Locate and identify every blood parasite.
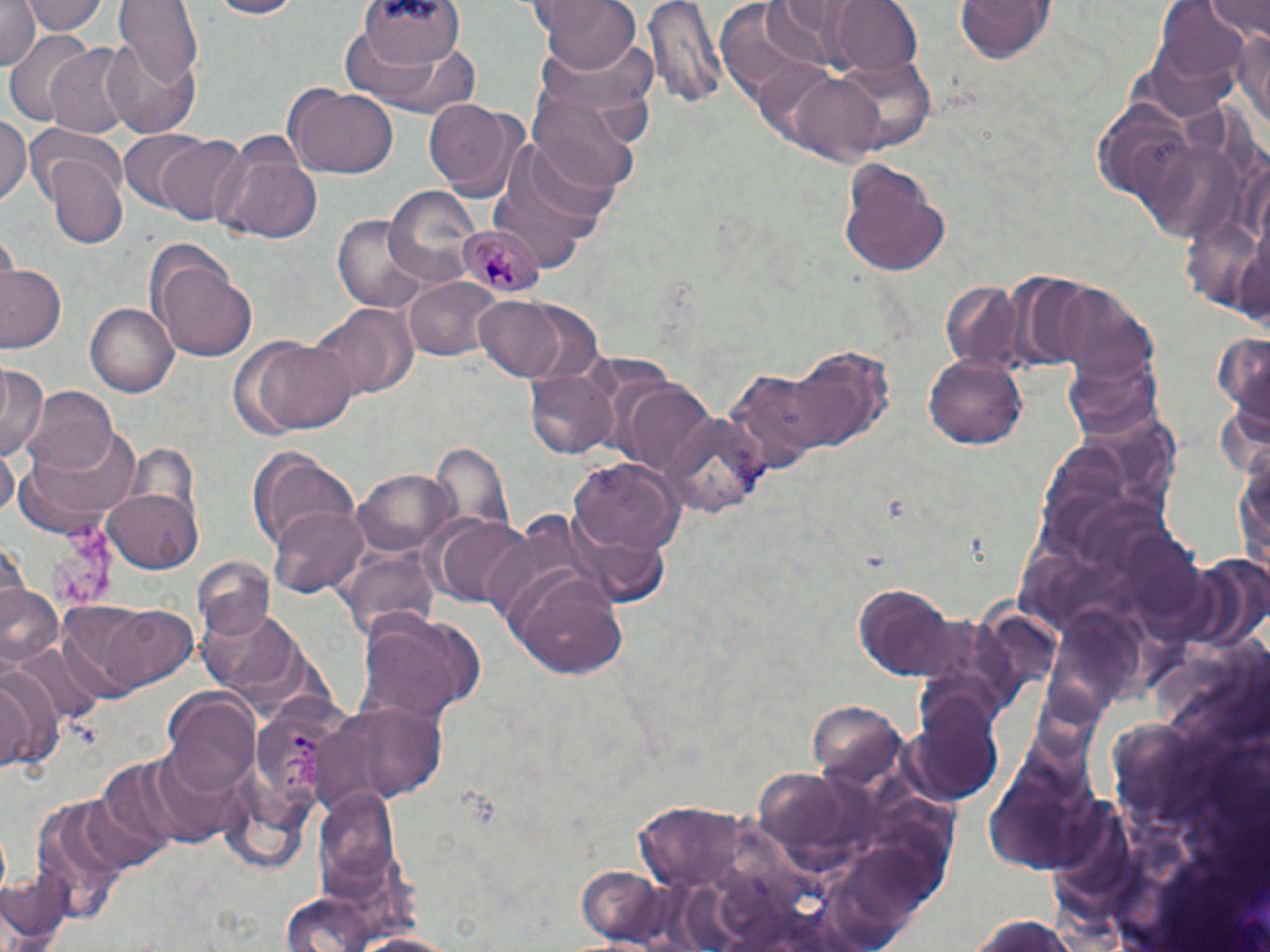
Approximate bounding boxes as named x1/y1/x2/y2 corners in pixels.
Plasmodium malariae-infected red blood cells: (x1=456, y1=224, x2=547, y2=302).
No Plasmodium falciparum, Plasmodium ovale, Plasmodium vivax, Babesia divergens, or Trypanosoma brucei observed.

Uninfected red blood cell locations: (x1=23, y1=0, x2=106, y2=37), (x1=114, y1=0, x2=202, y2=87), (x1=202, y1=0, x2=303, y2=19), (x1=358, y1=0, x2=463, y2=71), (x1=537, y1=0, x2=640, y2=73), (x1=647, y1=0, x2=725, y2=111), (x1=953, y1=0, x2=1057, y2=66), (x1=1157, y1=0, x2=1254, y2=83), (x1=1203, y1=0, x2=1270, y2=39), (x1=833, y1=1, x2=925, y2=75), (x1=0, y1=2, x2=40, y2=74), (x1=1232, y1=20, x2=1270, y2=134), (x1=4, y1=31, x2=101, y2=125), (x1=102, y1=33, x2=203, y2=142), (x1=349, y1=35, x2=480, y2=121), (x1=44, y1=44, x2=135, y2=141), (x1=834, y1=51, x2=939, y2=155), (x1=783, y1=71, x2=893, y2=166), (x1=286, y1=84, x2=399, y2=179), (x1=528, y1=93, x2=637, y2=198), (x1=423, y1=98, x2=517, y2=192), (x1=0, y1=116, x2=29, y2=209), (x1=25, y1=126, x2=123, y2=208), (x1=119, y1=131, x2=208, y2=208), (x1=156, y1=136, x2=247, y2=226), (x1=214, y1=144, x2=323, y2=244), (x1=47, y1=154, x2=129, y2=249), (x1=837, y1=159, x2=951, y2=277), (x1=386, y1=185, x2=482, y2=285), (x1=332, y1=217, x2=438, y2=313), (x1=156, y1=252, x2=258, y2=362), (x1=1, y1=264, x2=65, y2=353), (x1=403, y1=276, x2=501, y2=363), (x1=938, y1=280, x2=1024, y2=374), (x1=1048, y1=282, x2=1157, y2=384), (x1=471, y1=294, x2=573, y2=383), (x1=86, y1=303, x2=178, y2=397), (x1=313, y1=304, x2=419, y2=401), (x1=240, y1=332, x2=357, y2=437), (x1=1211, y1=334, x2=1270, y2=416), (x1=923, y1=353, x2=1027, y2=449), (x1=0, y1=365, x2=46, y2=460), (x1=525, y1=369, x2=619, y2=460), (x1=24, y1=390, x2=118, y2=478), (x1=14, y1=423, x2=146, y2=538), (x1=248, y1=445, x2=360, y2=561), (x1=0, y1=446, x2=18, y2=522), (x1=1234, y1=451, x2=1270, y2=578), (x1=569, y1=458, x2=680, y2=558), (x1=356, y1=467, x2=455, y2=557), (x1=104, y1=488, x2=202, y2=571), (x1=269, y1=505, x2=369, y2=599), (x1=435, y1=518, x2=535, y2=607), (x1=509, y1=573, x2=630, y2=682), (x1=851, y1=582, x2=960, y2=678), (x1=0, y1=585, x2=62, y2=670), (x1=96, y1=604, x2=199, y2=692), (x1=357, y1=610, x2=484, y2=723), (x1=0, y1=667, x2=57, y2=773), (x1=165, y1=694, x2=260, y2=797), (x1=316, y1=699, x2=451, y2=804), (x1=914, y1=700, x2=1005, y2=803), (x1=99, y1=749, x2=223, y2=856), (x1=1, y1=869, x2=72, y2=952), (x1=279, y1=897, x2=376, y2=952), (x1=960, y1=913, x2=1085, y2=952), (x1=348, y1=930, x2=463, y2=951). Slide-level diagnosis: Plasmodium malariae. Image is 1270×952 pixels. Thin blood film. May-Grünwald-Giemsa-stained preparation. Light microscopy. Captured at 1000x magnification. One field of a larger specimen.